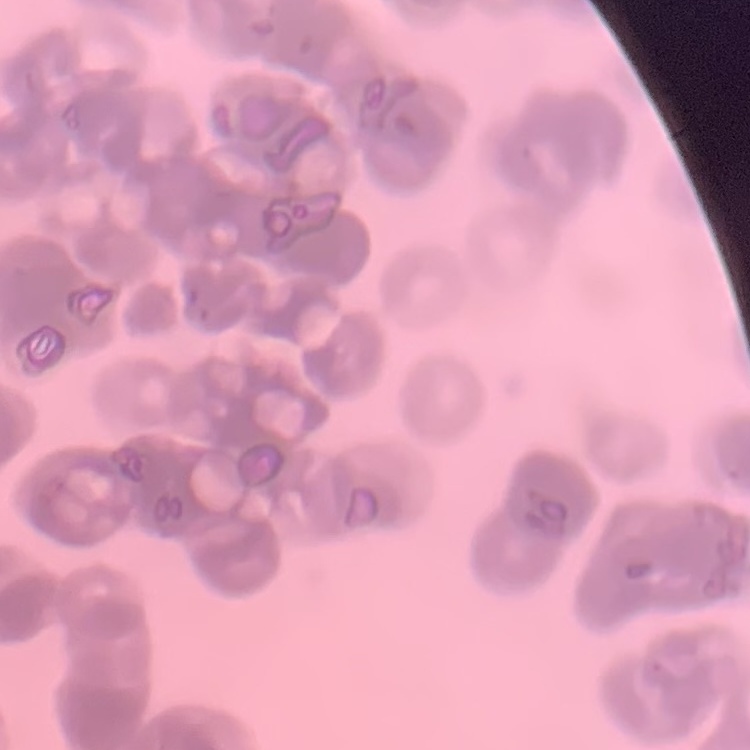
erythrocyte morphology = rouleaux formation
stain = Field's or Giemsa
image type = one tile cut from a larger photomicrograph
preparation = thin peripheral smear